Give the position of every malaria parasite and every leukocyte.
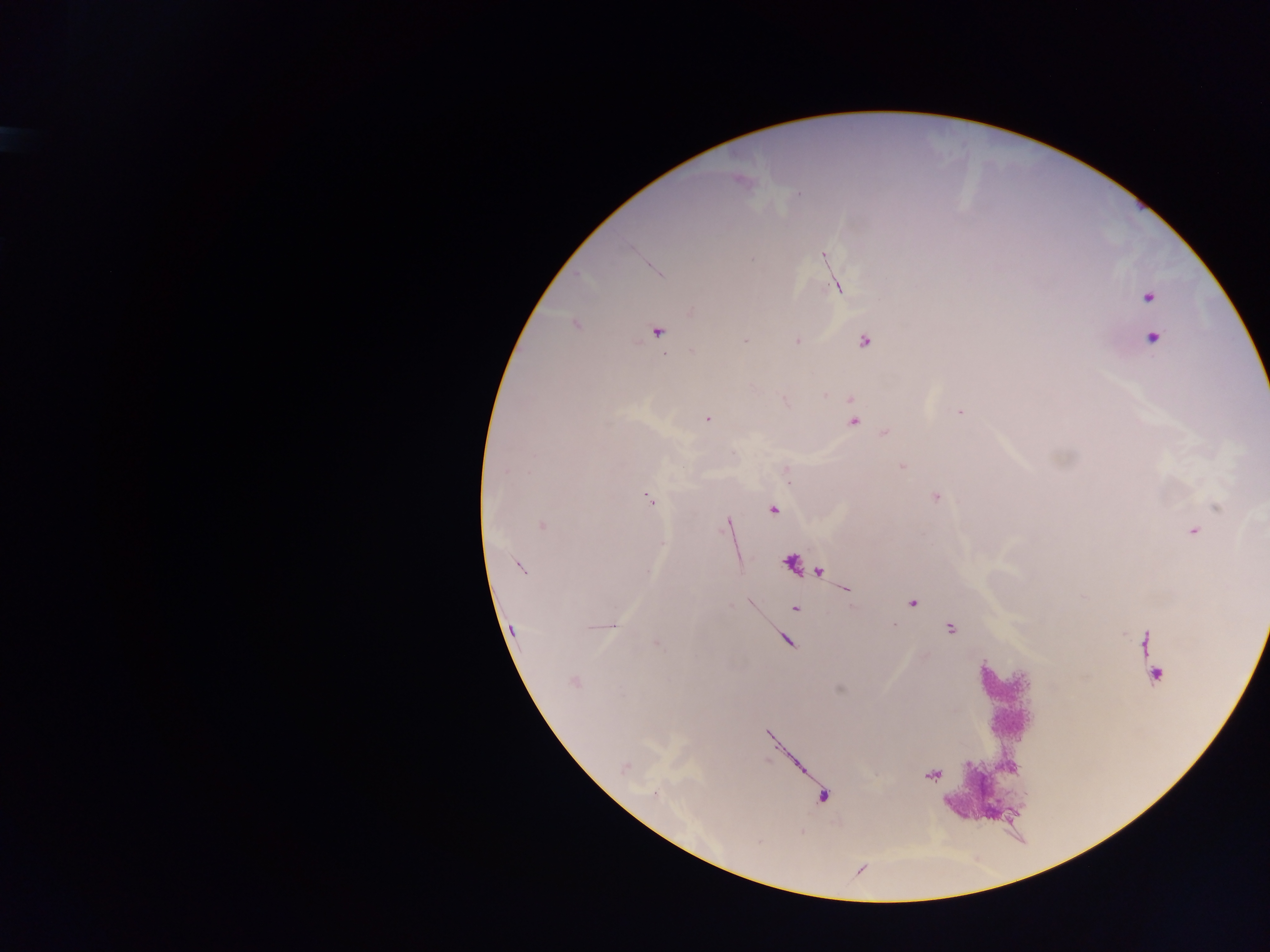
Approximate centers as {x, y} in pixels.
Malaria parasites: {823, 256}, {751, 259}, {837, 287}, {1148, 296}, {691, 312}, {576, 324}, {657, 333}, {1153, 338}, {745, 340}, {796, 341}, {864, 341}, {693, 351}, {960, 412}, {707, 418}, {853, 421}, {885, 433}, {902, 466}, {786, 470}, {505, 471}, {936, 497}, {649, 499}, {1218, 507}, {774, 509}, {726, 523}, {542, 525}, {1193, 531}, {520, 567}, {913, 603}, {796, 609}, {613, 625}, {950, 629}, {657, 644}, {1155, 675}, {574, 681}, {625, 767}, {655, 793}.
No leukocytes observed.

Thick blood smear. Collected in Ghana. Mobile-phone photograph taken through the microscope. Image is 1270×952 pixels. One field of view.